Assess this cell for malaria.
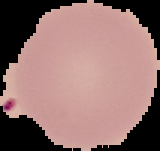

Uninfected.

The area outside the segmented cell region is set to black. Image is 160×151 pixels. From a thin blood smear.